Identify the cell.
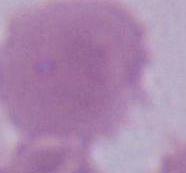

An erythrocyte.

{
  "magnification": "1000x",
  "modality": "photomicrograph"
}